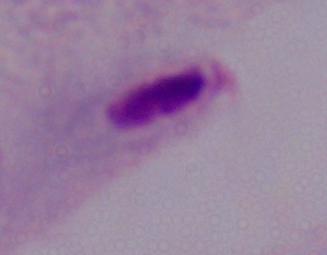 1000x magnification. Micrograph. A trichomonad is shown.